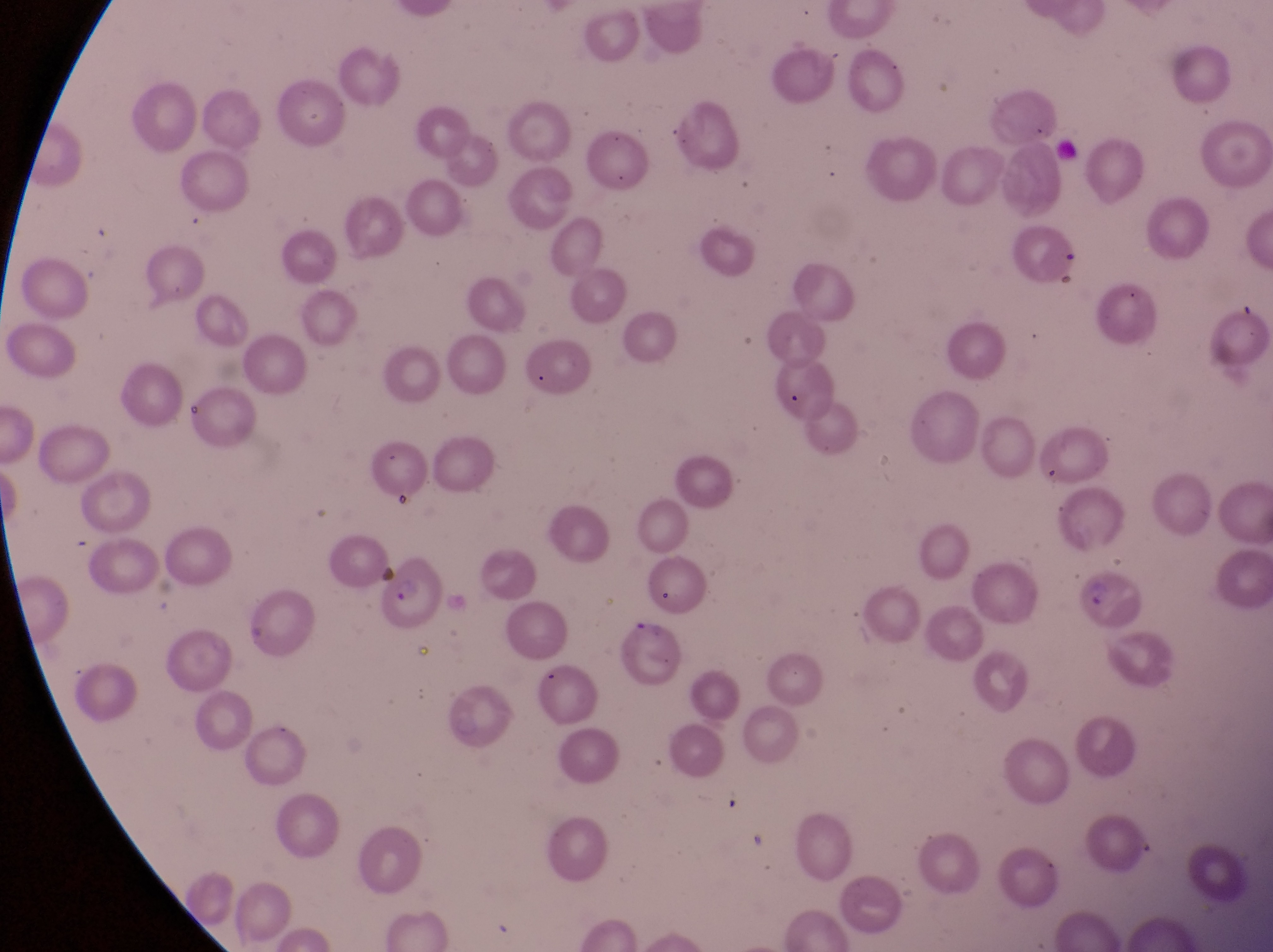
Approximate bounding boxes as [left, top, right, bottom] in pixels.
Summary:
  - Parasitised red blood cell locations: [377, 564, 447, 638], [1070, 570, 1144, 633], [618, 616, 689, 691]
  - Magnification: 1000x
  - Image size: 1273×952 pixels
  - Field of view: single
  - Preparation: thin blood smear
  - Capture: smartphone photograph through the eyepiece of an Olympus CX-23 microscope
  - Country: Uganda